Classify this cell by malaria status.
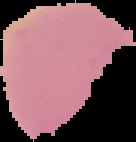
It is uninfected.

{
  "preparation": "thin blood smear",
  "image_size": "136×142 pixels",
  "image_type": "segmented cell region with the area outside set to black"
}